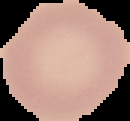

image_type: segmented cell region with the area outside set to black
image_size: 130×121 pixels
malaria_status: uninfected
preparation: thin blood smear